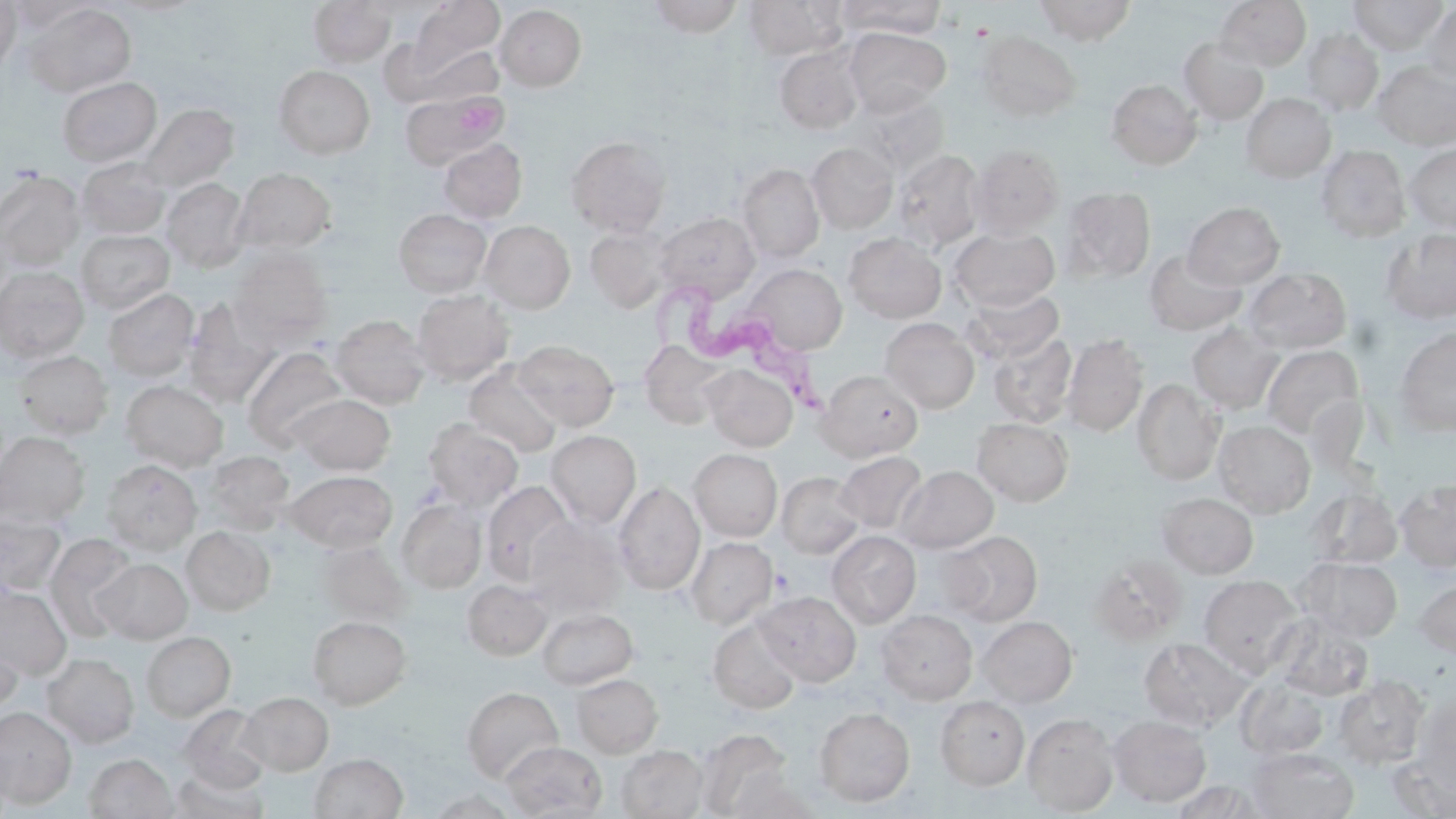 Approximate bounding boxes as (x1, y1, x2, y2) in pixels. Uninfected red blood cell locations: (0, 0, 21, 76), (646, 0, 745, 37), (743, 0, 848, 60), (836, 0, 948, 38), (1034, 0, 1138, 44), (1216, 0, 1311, 71), (1348, 0, 1449, 55), (5, 1, 96, 32), (308, 1, 396, 66), (408, 1, 504, 77), (24, 3, 136, 98), (1420, 4, 1455, 86), (495, 5, 587, 91), (843, 29, 950, 115), (1301, 29, 1384, 116), (978, 31, 1081, 122), (1178, 37, 1268, 125), (412, 44, 504, 106), (773, 45, 864, 134), (1374, 61, 1456, 150), (273, 65, 375, 159), (57, 77, 162, 167), (1106, 79, 1202, 169), (850, 93, 949, 176), (1241, 93, 1336, 182), (400, 94, 500, 168), (138, 104, 238, 193), (566, 135, 670, 237), (439, 139, 527, 223), (806, 143, 898, 232), (969, 144, 1064, 237), (1404, 144, 1456, 233), (1316, 145, 1410, 242), (892, 148, 985, 251), (76, 158, 170, 239), (737, 163, 824, 262), (234, 168, 336, 252), (0, 170, 83, 270), (162, 178, 249, 271), (1062, 186, 1156, 282), (1183, 202, 1285, 290), (394, 209, 491, 296), (654, 212, 759, 303), (480, 220, 575, 313), (584, 224, 673, 312), (949, 227, 1060, 311), (1382, 229, 1456, 324), (75, 230, 174, 314), (843, 233, 946, 323), (1144, 248, 1247, 335), (230, 249, 332, 343), (745, 264, 847, 356), (0, 267, 89, 363), (1243, 267, 1352, 354), (103, 288, 199, 381), (960, 288, 1063, 364), (412, 291, 515, 384), (184, 299, 278, 403), (330, 314, 429, 408), (880, 318, 980, 413), (1187, 322, 1284, 415), (1394, 328, 1456, 436), (987, 332, 1077, 428), (1062, 334, 1149, 437), (513, 340, 619, 430), (1261, 344, 1365, 442), (242, 348, 350, 450), (14, 350, 113, 439), (463, 361, 563, 458), (703, 364, 798, 451), (818, 370, 923, 461), (1132, 379, 1224, 485), (121, 380, 228, 471), (288, 394, 396, 475), (972, 417, 1073, 506), (424, 420, 523, 510), (1214, 420, 1315, 517), (545, 430, 641, 527), (0, 431, 90, 525), (689, 449, 783, 541), (205, 450, 294, 534), (834, 451, 928, 534), (102, 459, 202, 554), (896, 466, 998, 552), (285, 470, 398, 552), (776, 471, 865, 559), (1395, 479, 1456, 571), (481, 481, 574, 585), (614, 481, 705, 595), (1308, 486, 1402, 569), (1157, 492, 1258, 578), (397, 499, 487, 593), (0, 511, 66, 596), (525, 519, 624, 615), (181, 526, 274, 615), (827, 531, 921, 627), (942, 531, 1042, 626), (44, 533, 139, 641), (686, 537, 778, 629), (316, 540, 410, 626), (1091, 555, 1188, 644), (1298, 557, 1402, 641), (95, 558, 192, 643), (1199, 574, 1303, 674), (463, 579, 551, 660), (1415, 579, 1456, 660), (0, 586, 71, 678), (756, 591, 861, 686), (536, 607, 638, 689), (877, 609, 978, 704), (1271, 614, 1374, 701), (307, 615, 411, 709), (977, 616, 1077, 707), (708, 618, 802, 714), (0, 622, 23, 716), (141, 631, 235, 721), (1138, 638, 1250, 730), (42, 653, 139, 747), (572, 673, 663, 757), (1235, 676, 1332, 761), (1333, 676, 1429, 769), (461, 687, 563, 783), (239, 691, 333, 775), (1412, 694, 1456, 795), (935, 697, 1029, 790), (180, 704, 272, 794), (0, 707, 77, 808), (815, 707, 915, 806), (1023, 713, 1119, 815), (1109, 715, 1211, 806), (501, 741, 607, 818), (617, 745, 708, 819), (1247, 747, 1359, 819), (85, 753, 176, 818), (309, 753, 408, 819), (167, 766, 269, 818), (1169, 779, 1268, 818), (426, 790, 520, 818). Platelet locations: (452, 94, 507, 139). Trypanosoma brucei locations: (645, 283, 842, 422). Slide-level diagnosis: Trypanosoma brucei. May-Grünwald-Giemsa stain. Thin blood film. One field of a larger specimen. Image is 1456×819 pixels. Light microscopy. Captured at 1000x magnification.